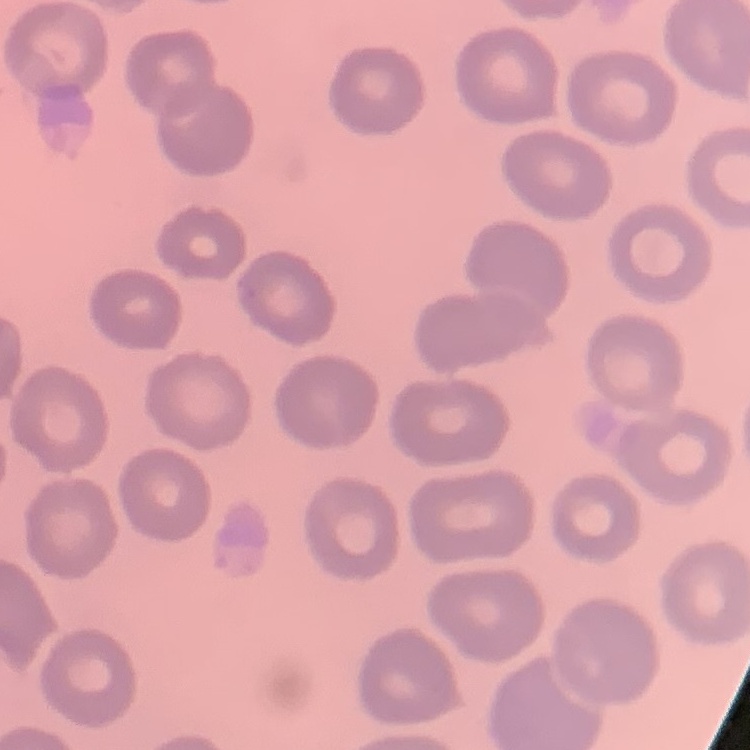
Summary:
  - Red blood cell morphology: no rouleaux formation
  - Stain: Field's or Giemsa
  - Preparation: thin blood smear
  - Image type: one tile cut from a larger photomicrograph